Assess this cell for malaria.
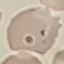
It is uninfected.

Summary:
  - Preparation: thin smear
  - Stain: Giemsa
  - Image type: automatically extracted cell patch, resized to 64 × 64 pixels
  - Capture: smartphone camera at the microscope eyepiece